Report the malaria status of this cell.
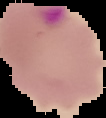

Parasitized.

Summary:
  - Image size: 106×118 pixels
  - Preparation: thin blood smear
  - Image type: segmented cell region on a black background